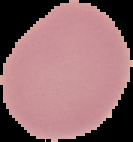
Summary:
  - Preparation: thin blood film
  - Result: negative for Plasmodium parasites
  - Image type: segmented cell region with the area outside set to black
  - Image size: 133×142 pixels